Report the malaria status of this cell.
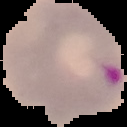

Parasitized.

image_size: 127×127 pixels
preparation: thin blood film
image_type: segmented cell region on a black background